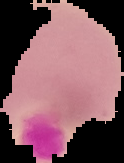

preparation = thin blood film
malaria status = uninfected
image type = segmented cell region with the area outside set to black
image size = 124×163 pixels